Locate every leukocyte (white blood cell).
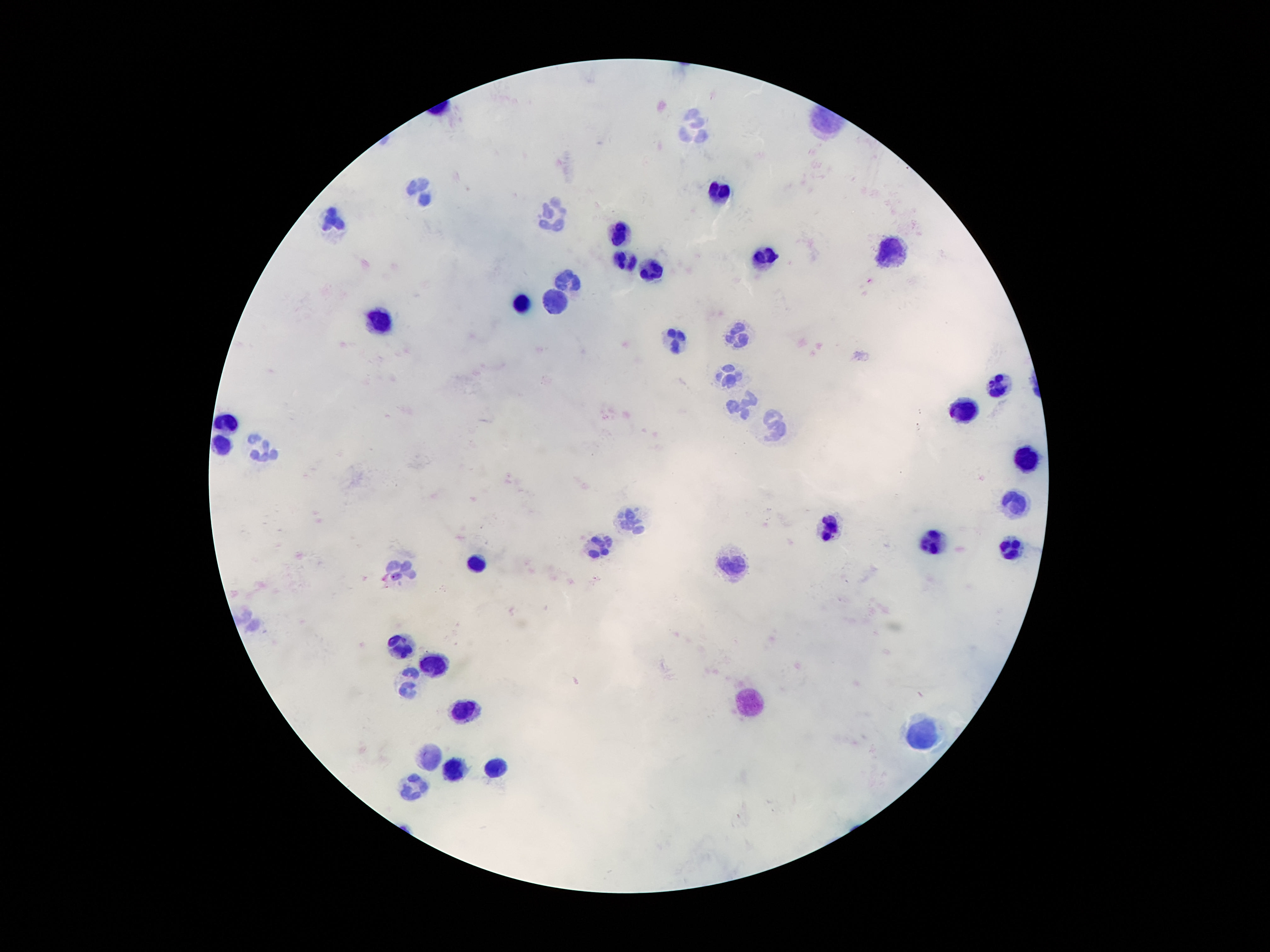
Approximate centers as (x, y) in pixels.
Leukocytes: (693, 122), (717, 192), (422, 193), (558, 215), (332, 218), (620, 233), (892, 254), (769, 258), (625, 259), (652, 269), (569, 277), (556, 299), (521, 302), (377, 318), (737, 334), (676, 340), (728, 378), (999, 388), (737, 409), (963, 411), (228, 422), (775, 430), (222, 443), (265, 447), (1027, 462), (1014, 502), (631, 519), (829, 527), (935, 538), (596, 544), (1012, 549), (476, 562), (736, 566), (401, 569), (398, 646), (433, 666), (407, 682), (749, 700), (463, 712), (920, 734), (429, 756), (497, 764), (452, 771), (413, 787).

Summary:
  - Image size: 1270×952 pixels
  - Magnification: 100x
  - Field of view: one from this slide
  - Preparation: thick blood film
  - Capture: smartphone camera through the microscope eyepiece
  - Stain: Giemsa
  - Patient malaria status: not infected